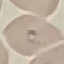

Result: malaria parasites detected. Thin blood smear. Giemsa-stained preparation. Automatically extracted cell patch, resized to 64 × 64 pixels. Photographed with a smartphone camera at the microscope eyepiece.